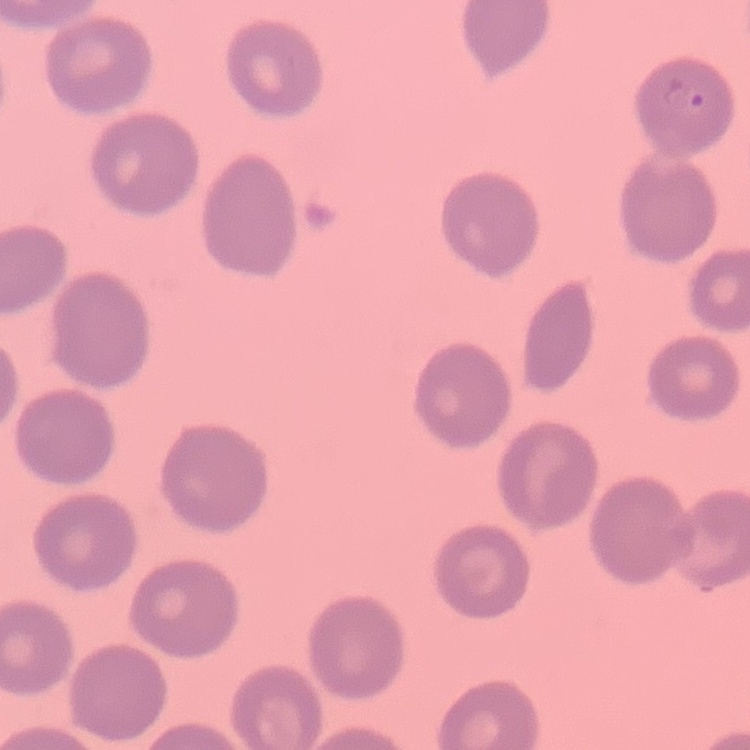
red blood cell morphology = no rouleaux formation
stain = Field's or Giemsa
preparation = thin blood film
image type = one tile cut from a larger photomicrograph